Report the malaria status of this cell.
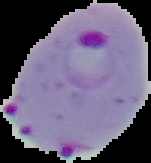

Parasitized.

Summary:
  - Image type: segmented cell region with the area outside set to black
  - Image size: 151×163 pixels
  - Preparation: thin blood film